Assess this cell for malaria.
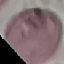
Uninfected.

Summary:
  - Image type: cell patch, automatically extracted from a larger field of view and resized to 64 × 64 pixels
  - Capture: smartphone camera at the microscope eyepiece
  - Preparation: thin blood smear
  - Stain: Giemsa